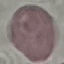
Result: no malaria parasites detected. Photographed with a smartphone camera at the microscope eyepiece. Giemsa stain. Cell patch, automatically extracted from a larger field of view and resized to 64 × 64 pixels. Thin smear of blood.